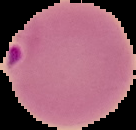 Image is 136×130 pixels. From a thin blood smear. The area outside the segmented cell region is set to black. Malaria status: parasitized.